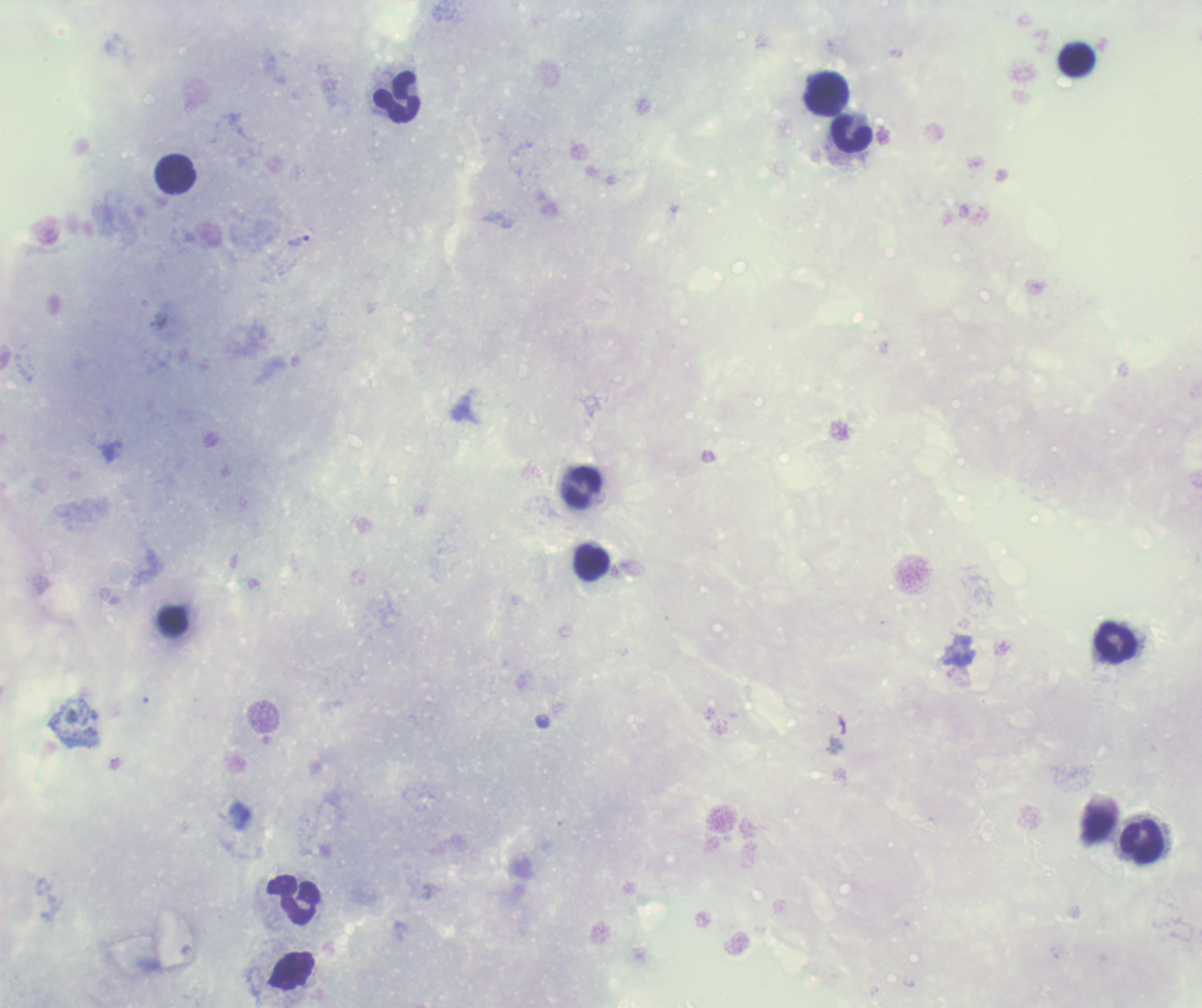

Approximate centers as {x, y} in pixels.
Summary:
  - Trophozoite locations: {299, 241}
  - Leukocyte locations: {1076, 60}, {825, 93}, {397, 97}, {852, 135}, {175, 173}, {581, 488}, {592, 564}, {172, 620}, {1116, 642}, {1141, 842}, {293, 899}
  - Magnification: 100x
  - Preparation: thick smear of blood
  - Stain: Romanowsky
  - Context: previously used in a real diagnosis
  - Background quality: poor
  - Coloration quality: bad
  - Field of view: one from this slide
  - Result: positive for Plasmodium parasites
  - Image size: 1202×1008 pixels